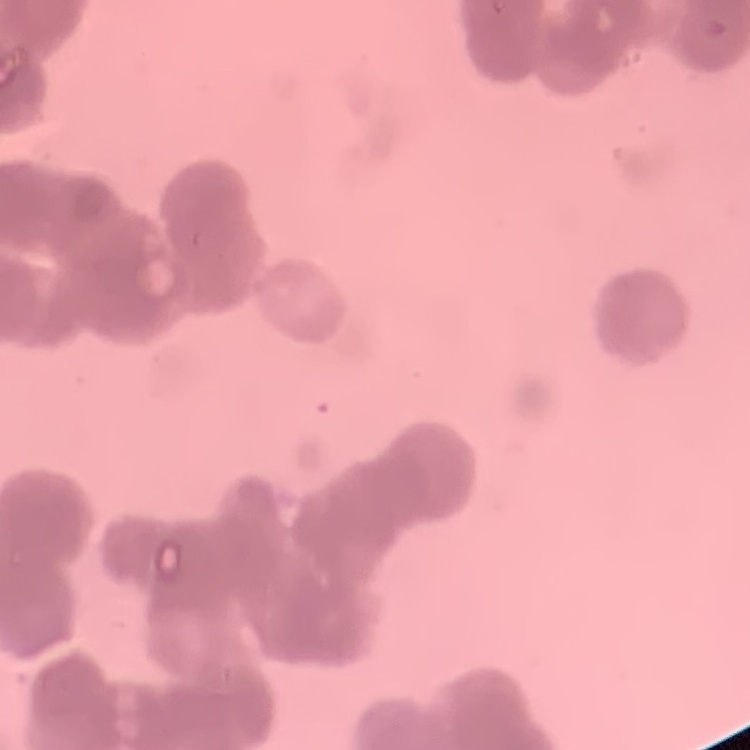

erythrocyte morphology = rouleaux formation
preparation = thin blood smear
image type = square crop of a larger photomicrograph
stain = Field's or Giemsa